Describe the morphology of the erythrocytes.
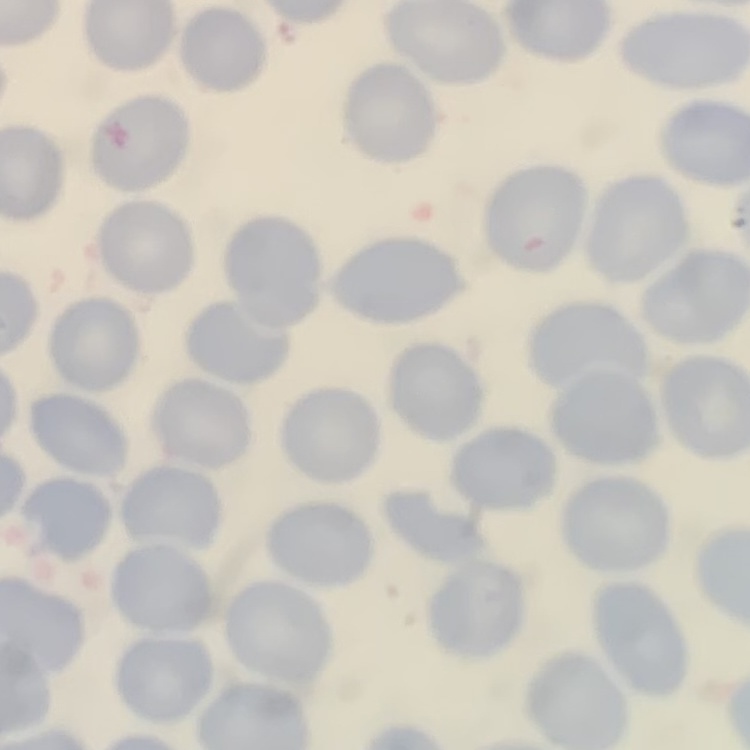

No rouleaux formation.

One tile cut from a larger photomicrograph. Field's or Giemsa stain. Thin peripheral smear.